Comment on the morphology of the red blood cells.
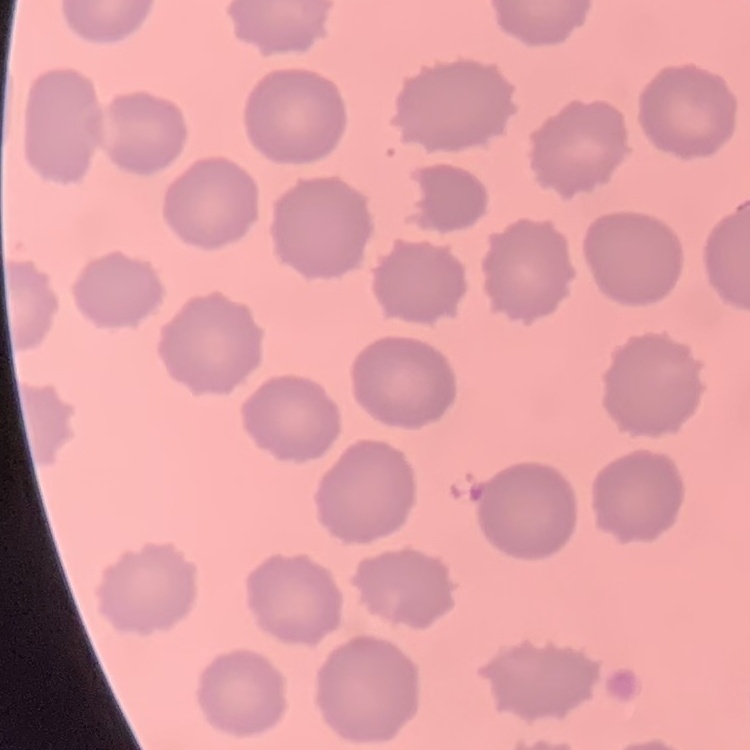
No rouleaux formation.

preparation: thin peripheral smear
image_type: square crop of a larger photomicrograph
stain: Field's or Giemsa